Assess this cell for malaria.
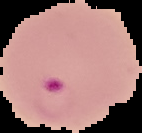
Parasitized.

Summary:
  - Preparation: thin blood film
  - Image type: segmented cell region with the area outside set to black
  - Image size: 142×133 pixels